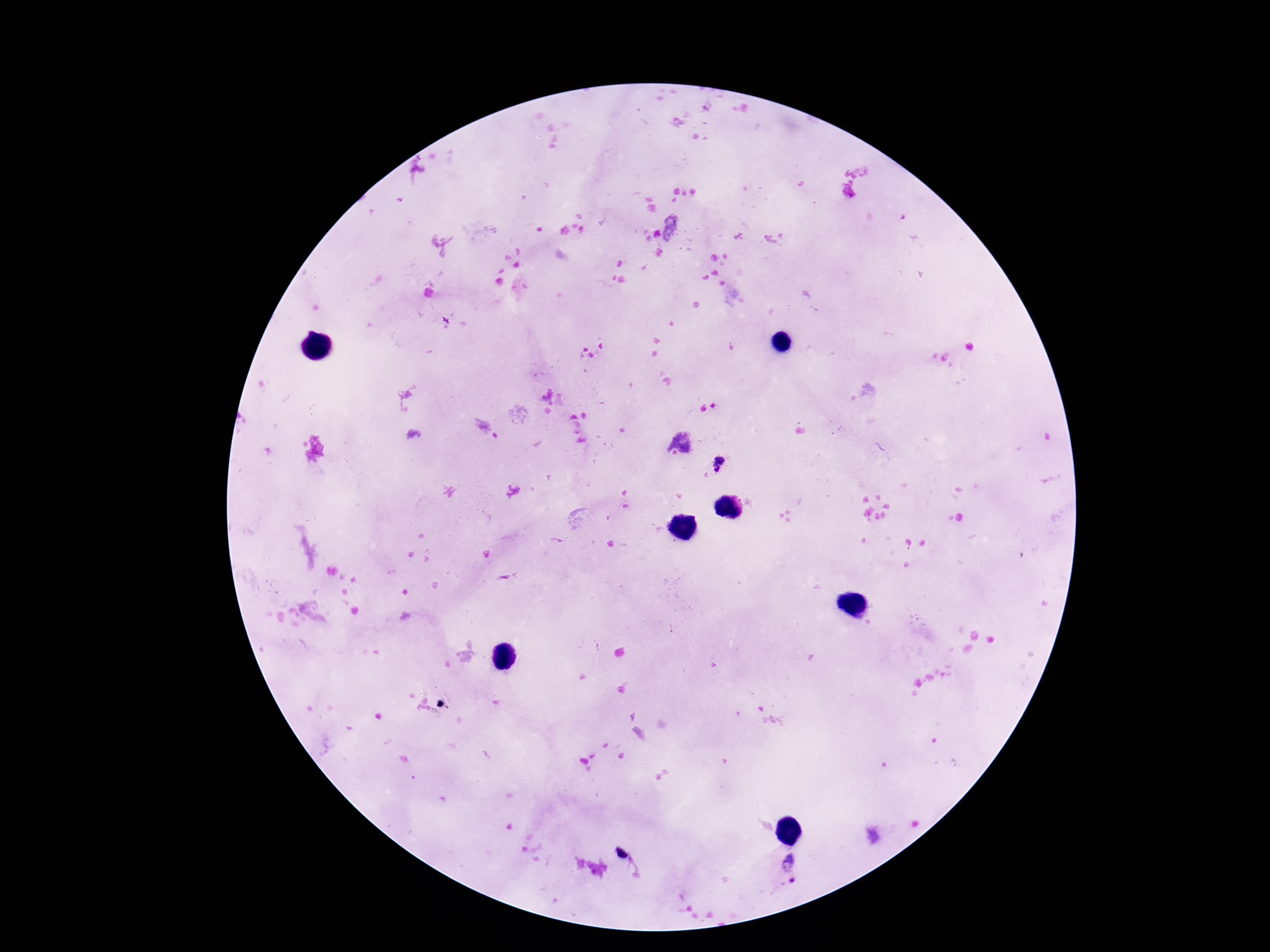

{
  "patient_malaria_status": "positive",
  "magnification": "100x",
  "preparation": "thick peripheral-blood smear",
  "capture": "smartphone camera through the microscope eyepiece",
  "stain": "Giemsa",
  "field_of_view": "one from this slide",
  "image_size": "1270×952 pixels",
  "plasmodium_parasite_locations": "approximate object centers, in pixels from the top-left corner: (x=719, y=464), (x=795, y=869)"
}